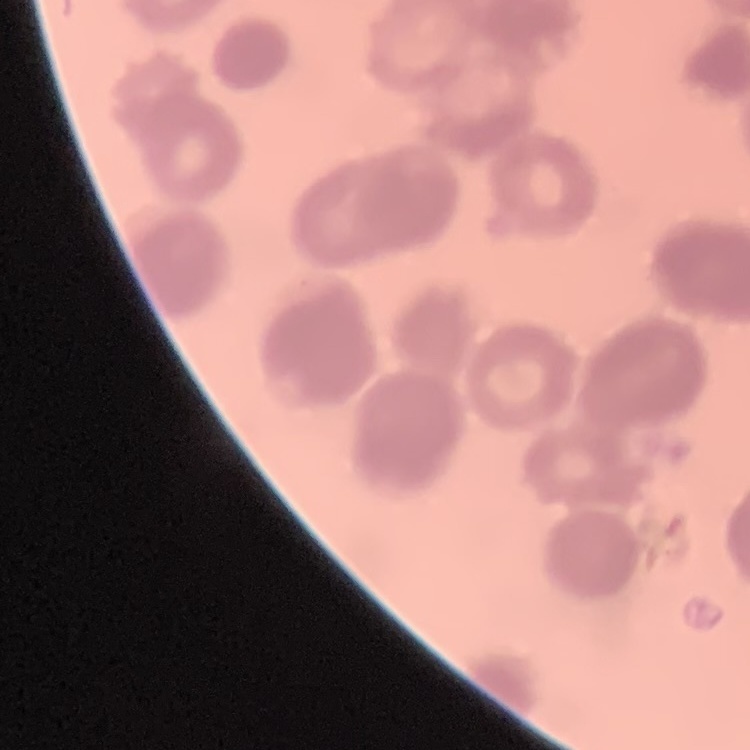

{
  "red_blood_cell_morphology": "rouleaux formation",
  "preparation": "thin peripheral smear",
  "image_type": "square crop of a larger photomicrograph",
  "stain": "Field's or Giemsa"
}